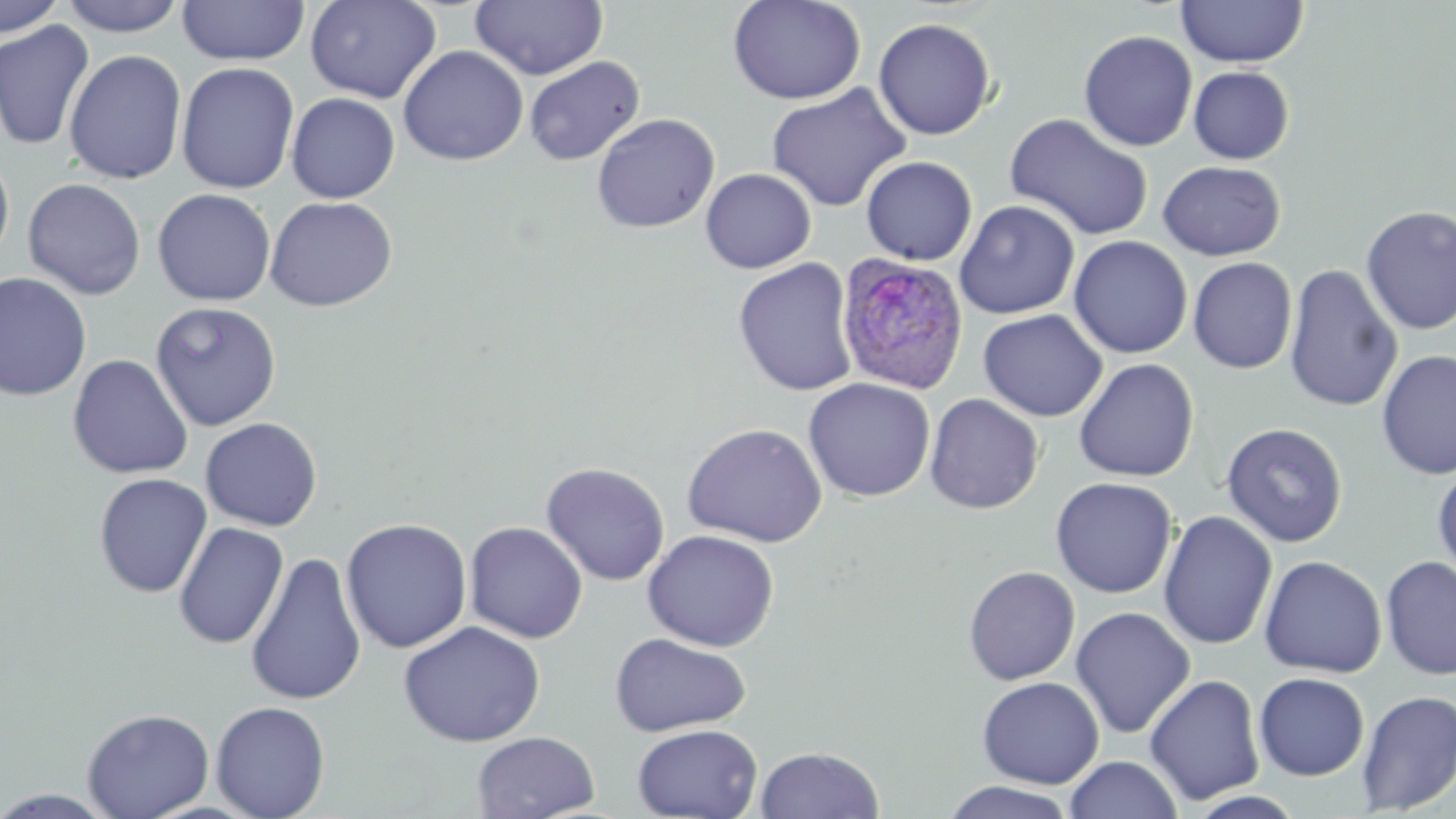
Summary:
  - Coordinate format: approximate bounding boxes as [x1, y1, x2, y2] in pixels
  - Plasmodium ovale-infected red blood cell locations: [835, 252, 969, 395]
  - Uninfected red blood cell locations: [0, 0, 68, 39], [56, 0, 190, 37], [306, 0, 441, 104], [471, 0, 607, 81], [727, 0, 866, 105], [1176, 0, 1309, 68], [176, 1, 309, 66], [873, 17, 996, 140], [0, 20, 95, 150], [1078, 30, 1198, 152], [398, 45, 529, 166], [64, 49, 187, 184], [524, 56, 645, 166], [176, 61, 300, 194], [1188, 66, 1294, 164], [765, 83, 912, 213], [286, 93, 400, 203], [591, 113, 720, 233], [1004, 113, 1154, 241], [0, 148, 15, 269], [861, 155, 978, 266], [1158, 160, 1285, 261], [700, 168, 816, 273], [22, 178, 146, 300], [152, 188, 277, 305], [264, 195, 398, 312], [955, 200, 1080, 319], [1360, 205, 1456, 335], [1068, 235, 1192, 359], [733, 257, 859, 396], [1187, 257, 1297, 374], [1284, 265, 1402, 413], [0, 272, 93, 401], [149, 301, 282, 432], [978, 309, 1107, 422], [1376, 349, 1456, 480], [67, 354, 193, 479], [1073, 359, 1200, 482], [803, 377, 936, 502], [924, 393, 1044, 514], [200, 417, 323, 531], [682, 422, 827, 547], [1220, 422, 1348, 547], [540, 462, 670, 586], [1432, 462, 1456, 583], [93, 472, 212, 598], [1050, 477, 1177, 598], [1157, 510, 1277, 650], [340, 518, 472, 653], [173, 521, 289, 650], [465, 521, 588, 644], [641, 529, 780, 651], [245, 551, 367, 707], [1259, 554, 1387, 678], [1381, 554, 1456, 680], [962, 565, 1081, 685], [1069, 606, 1196, 738], [398, 621, 545, 746], [610, 632, 752, 736], [1253, 672, 1370, 780], [1144, 673, 1265, 806], [977, 676, 1103, 789], [1356, 689, 1456, 815], [211, 700, 331, 819], [81, 707, 215, 819], [632, 723, 764, 819], [472, 731, 600, 818], [756, 746, 884, 818], [1065, 755, 1182, 819], [938, 780, 1079, 819], [0, 788, 120, 819]
  - Slide-level diagnosis: Plasmodium ovale
  - Magnification: 1000x
  - Image size: 1456×819 pixels
  - Stain: May-Grünwald-Giemsa
  - Field of view: single
  - Modality: optical microscopy
  - Preparation: thin blood film